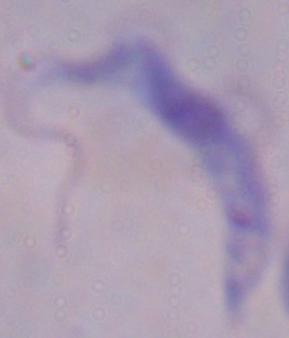
modality: photomicrograph
magnification: 1000x
identification: trypanosome